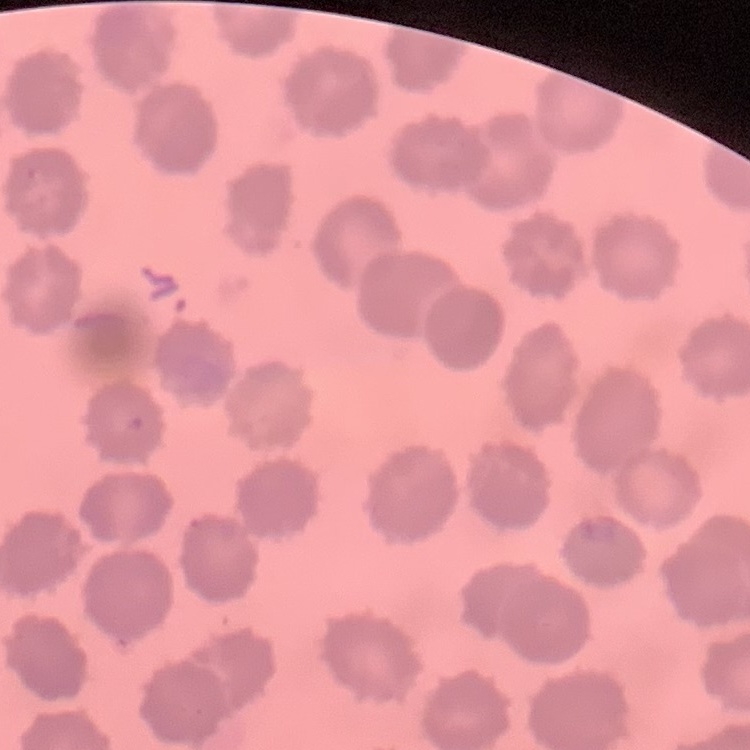

red blood cell morphology = no rouleaux formation
preparation = thin blood film
stain = Field's or Giemsa
image type = square crop of a larger photomicrograph